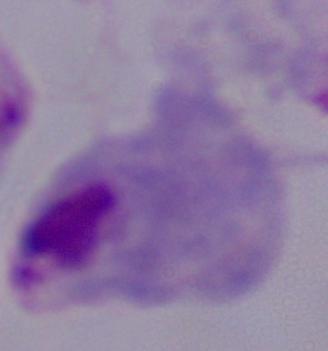

identification = trichomonad
modality = micrograph
magnification = 1000x